Assess this cell for malaria.
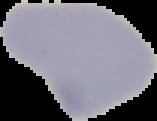

Uninfected.

Summary:
  - Preparation: thin blood smear
  - Image type: cell region segmented out of the field of view; surrounding area masked to black
  - Image size: 157×121 pixels